Mark where platelets are.
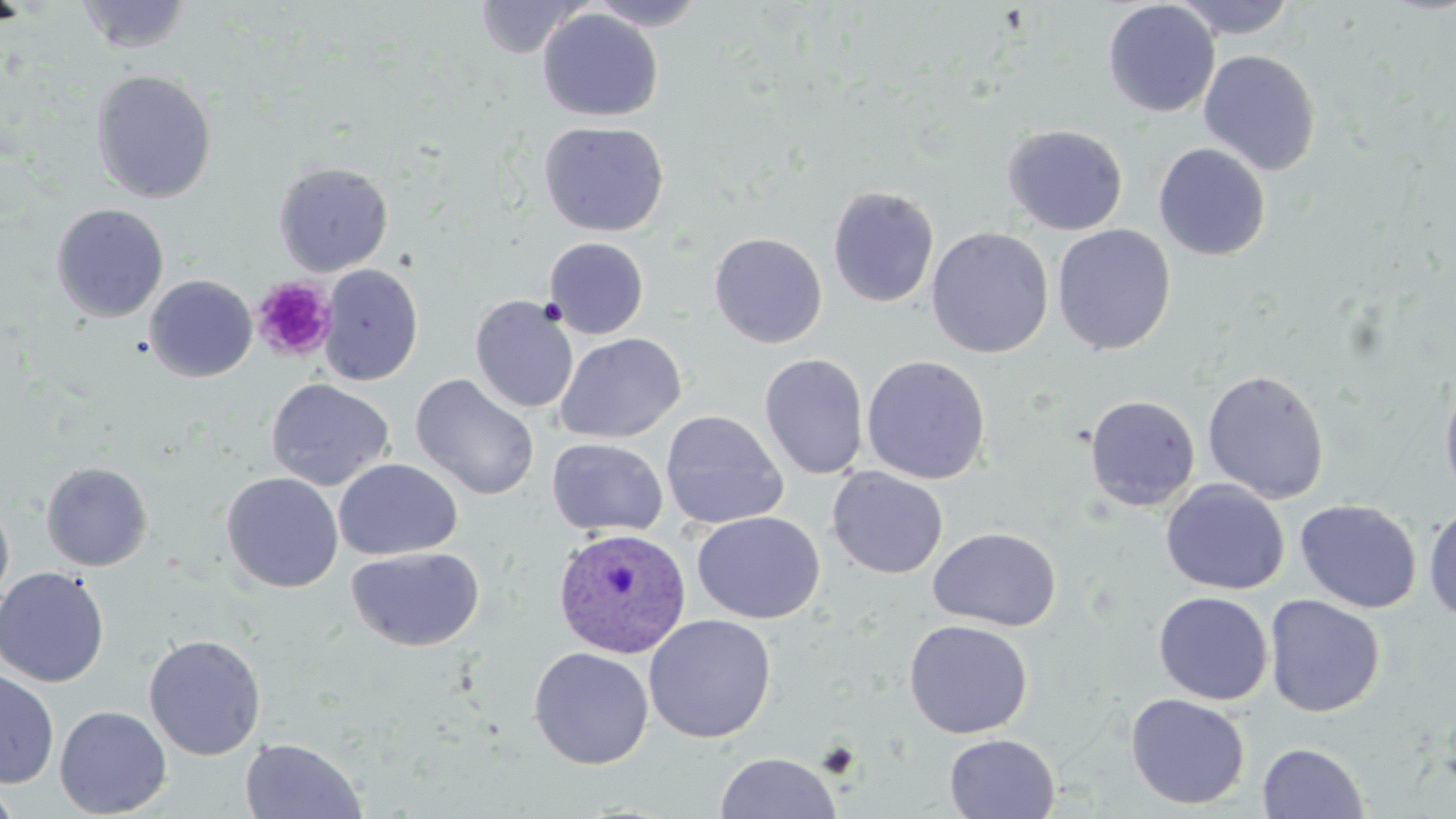

Approximate bounding boxes as [x1, y1, x2, y2] in pixels.
Platelets: [251, 277, 337, 362].

Plasmodium ovale-infected red blood cell locations = approximate bounding boxes as [x1, y1, x2, y2] in pixels: [553, 527, 692, 659]
slide-level diagnosis = Plasmodium ovale
stain = May-Grünwald-Giemsa
field of view = single
modality = light microscopy
uninfected red blood cell locations = approximate bounding boxes as [x1, y1, x2, y2] in pixels: [76, 0, 194, 54], [475, 0, 591, 59], [585, 0, 710, 30], [1171, 0, 1299, 39], [1102, 1, 1220, 118], [537, 8, 663, 122], [1198, 49, 1322, 176], [90, 69, 217, 204], [538, 121, 669, 237], [1002, 124, 1128, 236], [1153, 143, 1271, 261], [273, 161, 393, 276], [826, 186, 940, 308], [51, 204, 169, 323], [1051, 224, 1176, 355], [926, 227, 1054, 358], [709, 232, 827, 348], [544, 236, 649, 339], [318, 264, 423, 386], [144, 275, 257, 382], [470, 295, 579, 414], [554, 332, 686, 443], [759, 353, 870, 480], [861, 355, 991, 485], [1202, 370, 1330, 504], [1438, 373, 1456, 510], [410, 374, 540, 500], [265, 378, 394, 491], [1083, 394, 1201, 511], [660, 410, 789, 530], [546, 437, 669, 537], [334, 458, 462, 560], [41, 461, 153, 571], [827, 467, 948, 578], [221, 472, 343, 593], [1160, 480, 1289, 595], [0, 494, 15, 613], [1295, 499, 1422, 614], [1422, 503, 1456, 625], [691, 511, 825, 625], [928, 527, 1061, 631], [346, 546, 485, 652], [0, 566, 109, 687], [1153, 591, 1273, 705], [1264, 595, 1385, 717], [643, 614, 777, 744], [903, 619, 1033, 739], [143, 633, 266, 760], [529, 646, 654, 770], [0, 667, 59, 788], [1125, 693, 1251, 810], [54, 705, 172, 818], [944, 733, 1061, 819], [239, 737, 367, 818], [1257, 742, 1369, 818], [714, 751, 842, 819], [0, 780, 21, 819]
magnification = 1000x
preparation = thin blood film
image size = 1456×819 pixels